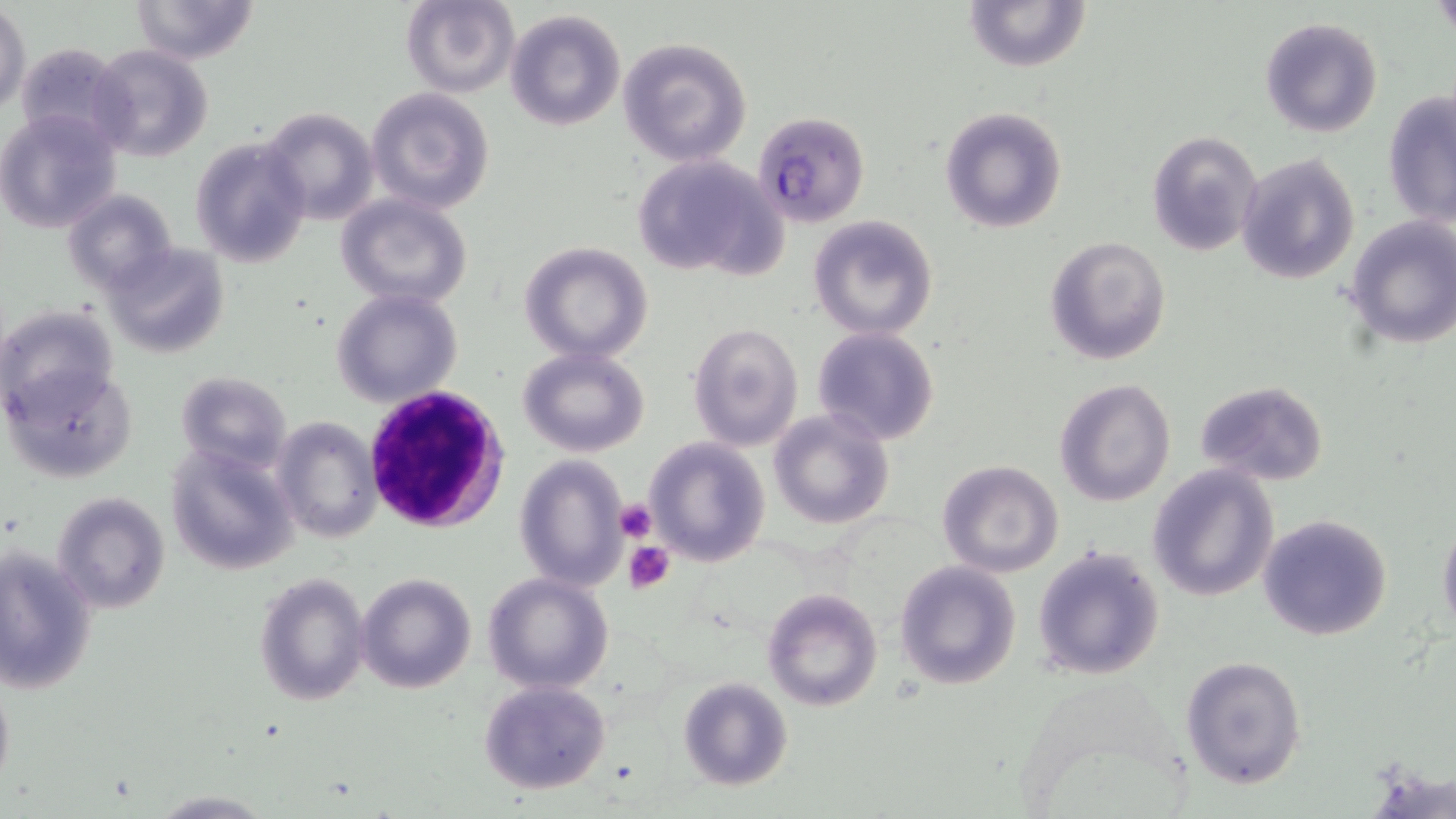

Summary:
  - Coordinate format: approximate bounding boxes as named x1/y1/x2/y2 corners in pixels
  - Platelet locations: (x1=612, y1=498, x2=659, y2=544), (x1=623, y1=539, x2=677, y2=593)
  - Uninfected red blood cell locations: (x1=130, y1=0, x2=258, y2=64), (x1=400, y1=0, x2=521, y2=98), (x1=961, y1=1, x2=1091, y2=75), (x1=0, y1=5, x2=30, y2=113), (x1=505, y1=8, x2=628, y2=132), (x1=1260, y1=16, x2=1382, y2=137), (x1=615, y1=37, x2=752, y2=167), (x1=14, y1=40, x2=129, y2=148), (x1=89, y1=45, x2=214, y2=164), (x1=367, y1=88, x2=494, y2=214), (x1=1382, y1=92, x2=1456, y2=227), (x1=939, y1=103, x2=1068, y2=234), (x1=259, y1=107, x2=377, y2=223), (x1=0, y1=108, x2=124, y2=232), (x1=1146, y1=129, x2=1261, y2=256), (x1=189, y1=136, x2=312, y2=269), (x1=1235, y1=152, x2=1362, y2=285), (x1=631, y1=154, x2=782, y2=276), (x1=63, y1=189, x2=177, y2=298), (x1=337, y1=193, x2=475, y2=308), (x1=808, y1=215, x2=938, y2=341), (x1=1345, y1=216, x2=1456, y2=350), (x1=1044, y1=236, x2=1171, y2=364), (x1=103, y1=241, x2=230, y2=360), (x1=520, y1=242, x2=654, y2=364), (x1=331, y1=289, x2=463, y2=406), (x1=2, y1=304, x2=121, y2=421), (x1=687, y1=320, x2=806, y2=452), (x1=812, y1=326, x2=941, y2=446), (x1=518, y1=347, x2=651, y2=458), (x1=7, y1=362, x2=136, y2=483), (x1=175, y1=372, x2=291, y2=474), (x1=1054, y1=379, x2=1176, y2=506), (x1=1194, y1=380, x2=1329, y2=486), (x1=767, y1=409, x2=895, y2=530), (x1=272, y1=416, x2=382, y2=542), (x1=645, y1=438, x2=768, y2=567), (x1=166, y1=441, x2=298, y2=573), (x1=514, y1=455, x2=630, y2=592), (x1=937, y1=460, x2=1064, y2=578), (x1=1146, y1=465, x2=1277, y2=601), (x1=53, y1=490, x2=170, y2=614), (x1=1258, y1=514, x2=1392, y2=643), (x1=1438, y1=516, x2=1456, y2=635), (x1=1032, y1=544, x2=1166, y2=683), (x1=1, y1=545, x2=97, y2=696), (x1=895, y1=561, x2=1019, y2=689), (x1=255, y1=571, x2=370, y2=706), (x1=356, y1=572, x2=478, y2=694), (x1=483, y1=572, x2=614, y2=695), (x1=763, y1=588, x2=884, y2=712), (x1=1180, y1=656, x2=1306, y2=790), (x1=0, y1=673, x2=14, y2=799), (x1=678, y1=677, x2=793, y2=790), (x1=479, y1=681, x2=612, y2=796)
  - Plasmodium falciparum-infected red blood cell locations: (x1=752, y1=110, x2=870, y2=226)
  - White blood cell locations: (x1=361, y1=385, x2=509, y2=536)
  - Slide-level diagnosis: Plasmodium falciparum
  - Magnification: 1000x
  - Stain: May-Grünwald-Giemsa
  - Field of view: one of a larger specimen
  - Modality: optical microscopy
  - Preparation: thin blood smear
  - Image size: 1456×819 pixels